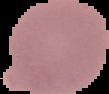
Summary:
  - Preparation: thin blood film
  - Image size: 109×94 pixels
  - Image type: segmented cell region with the area outside set to black
  - Result: negative for malaria parasites